Classify this cell by malaria status.
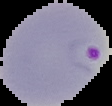
It is parasitized.

From a thin blood smear. The area outside the segmented cell region is set to black. Image is 112×106 pixels.